Name the blood parasite species.
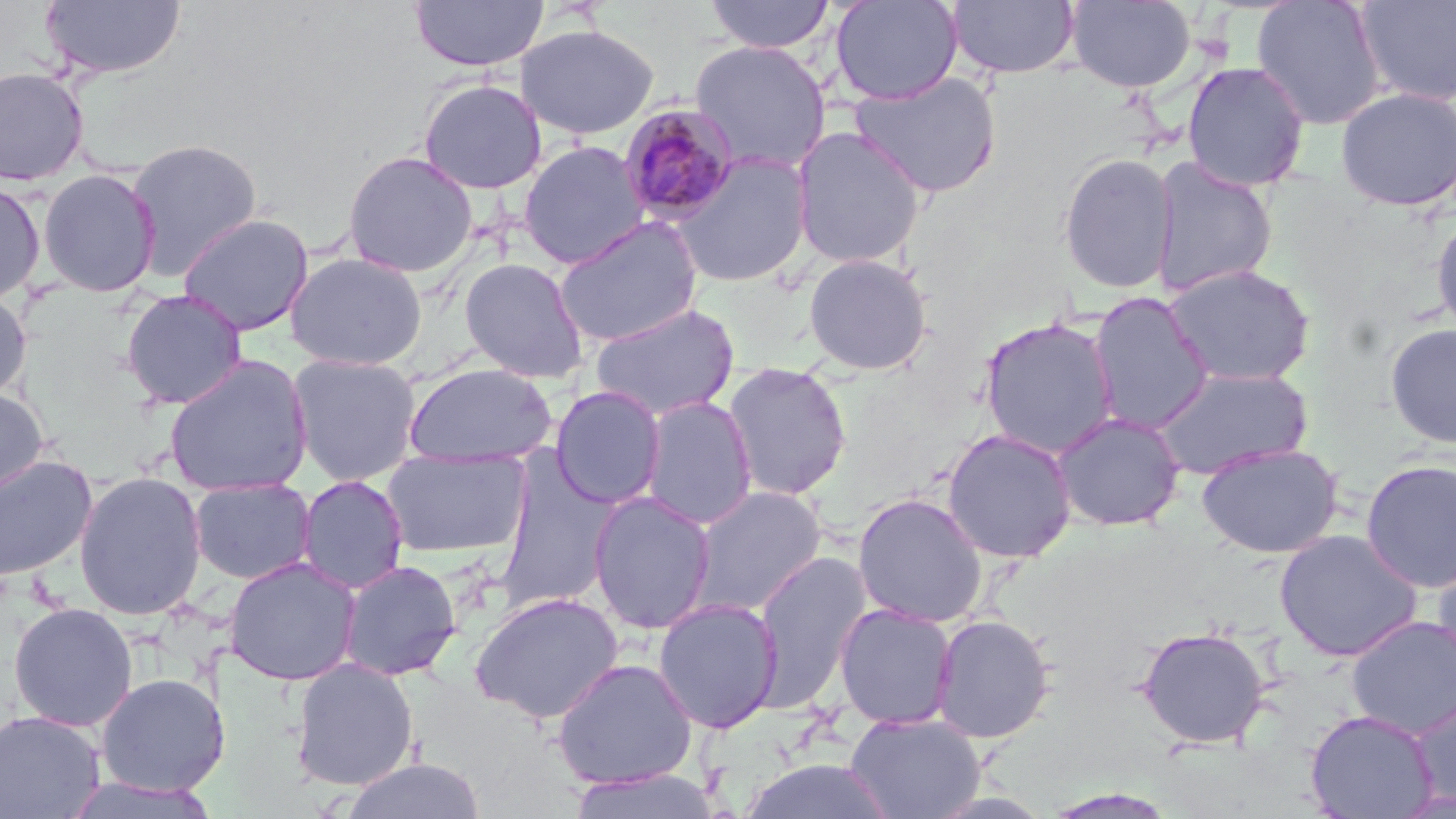
Plasmodium malariae.

Summary:
  - Coordinate format: approximate bounding boxes as (x1, y1, x2, y2) in pixels
  - Plasmodium malariae-infected red blood cell locations: (619, 102, 741, 226)
  - Uninfected red blood cell locations: (40, 0, 187, 80), (409, 0, 549, 72), (704, 0, 836, 54), (831, 0, 963, 105), (1251, 0, 1386, 129), (946, 1, 1079, 79), (1066, 1, 1195, 93), (1355, 1, 1456, 106), (516, 23, 659, 139), (689, 39, 831, 174), (1182, 61, 1310, 191), (0, 66, 90, 187), (850, 70, 1003, 198), (419, 79, 547, 194), (1335, 87, 1456, 212), (791, 125, 927, 269), (125, 138, 264, 279), (517, 140, 650, 269), (342, 150, 479, 277), (666, 151, 814, 288), (1058, 152, 1178, 294), (1149, 157, 1277, 298), (37, 168, 161, 298), (0, 179, 46, 304), (1431, 209, 1456, 339), (179, 213, 314, 336), (553, 216, 703, 348), (285, 251, 427, 371), (803, 253, 933, 376), (458, 257, 589, 382), (1162, 263, 1316, 387), (0, 288, 31, 401), (121, 289, 247, 409), (1087, 292, 1215, 435), (589, 302, 741, 421), (979, 316, 1120, 458), (1385, 323, 1456, 449), (288, 353, 422, 487), (164, 355, 313, 496), (722, 362, 853, 501), (403, 363, 557, 467), (1150, 366, 1313, 480), (550, 385, 666, 509), (0, 387, 49, 497), (640, 395, 757, 529), (1051, 412, 1186, 532), (941, 428, 1077, 563), (1196, 442, 1344, 558), (381, 447, 530, 559), (0, 454, 98, 581), (497, 456, 619, 610), (1360, 459, 1456, 593), (73, 471, 207, 620), (297, 475, 409, 594), (190, 477, 316, 585), (689, 486, 827, 616), (588, 491, 716, 635), (852, 492, 988, 628), (1274, 529, 1424, 662), (1431, 542, 1456, 679), (751, 550, 872, 711), (223, 557, 361, 685), (339, 560, 462, 681), (470, 591, 624, 723), (653, 598, 783, 733), (8, 602, 138, 731), (834, 603, 957, 730), (931, 614, 1056, 743), (1346, 615, 1456, 738), (1137, 625, 1270, 749), (551, 657, 698, 790), (290, 658, 419, 790), (94, 672, 229, 796), (1407, 695, 1456, 811), (1305, 709, 1438, 819), (0, 710, 106, 819), (845, 712, 985, 819), (339, 758, 486, 819), (740, 758, 896, 818), (564, 767, 724, 819), (62, 776, 220, 817), (1041, 788, 1180, 818)
  - Stain: May-Grünwald-Giemsa
  - Modality: light microscopy
  - Field of view: single
  - Magnification: 1000x
  - Preparation: thin blood smear
  - Image size: 1456×819 pixels